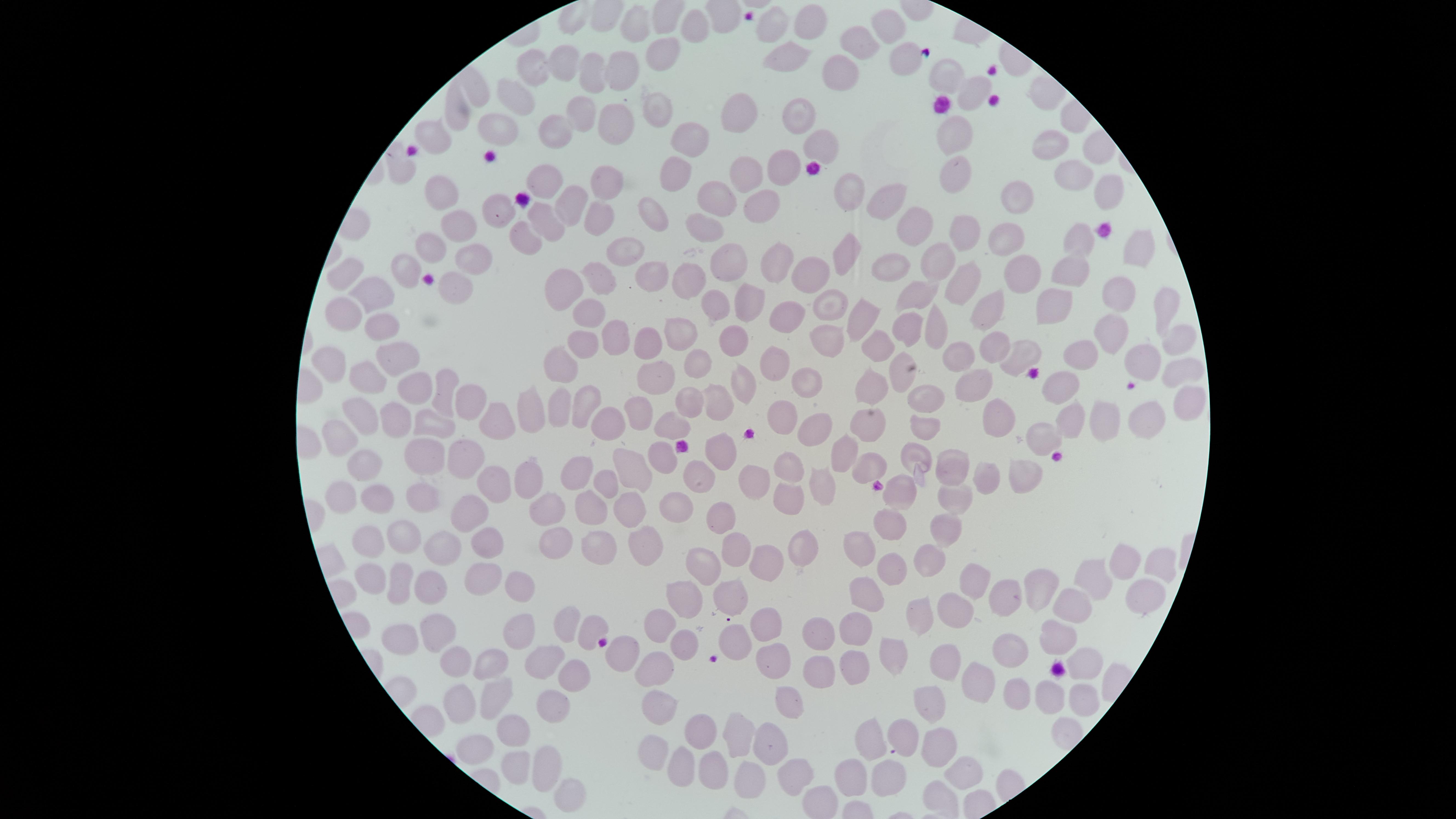

visible region = circular
stain = Giemsa
uninfected RBCs = approximate marker points as (x, y) in pixels: (807, 21), (890, 21), (777, 22), (693, 23), (634, 24), (857, 40), (661, 50), (794, 58), (905, 59), (563, 63), (538, 68), (620, 68), (591, 73), (842, 73), (946, 74), (516, 91), (971, 96), (650, 103), (581, 108), (739, 108), (455, 114), (797, 115), (553, 124), (608, 124), (495, 129), (690, 133), (947, 134), (440, 137), (823, 143), (1051, 145), (401, 166), (784, 169), (746, 174), (955, 175), (677, 177), (1069, 177), (540, 178), (610, 184), (440, 186), (1023, 193), (1113, 194), (719, 196), (840, 196), (761, 199), (879, 201), (570, 203), (502, 205), (654, 214), (548, 218), (599, 218), (915, 219), (459, 226), (709, 229), (1004, 232), (962, 235), (525, 238), (1079, 243), (624, 248), (432, 249), (1136, 253), (476, 256), (847, 256), (936, 256), (727, 261), (776, 262), (893, 267), (1020, 269), (1069, 271), (405, 272), (652, 273), (807, 273), (348, 275), (693, 278), (459, 282), (603, 282), (566, 287), (958, 288), (1116, 293), (372, 295), (922, 296), (838, 302), (1064, 302), (751, 303), (344, 305), (989, 305), (720, 306), (1167, 309), (595, 310), (867, 314), (792, 318), (379, 321), (936, 325), (680, 333), (907, 333), (616, 336), (1114, 337), (737, 338), (1177, 339), (826, 340), (582, 342), (643, 342), (877, 347), (995, 348), (398, 350), (960, 350), (333, 358), (778, 358), (1019, 358), (1085, 358), (700, 362), (1142, 363), (562, 366), (901, 368), (369, 374), (656, 374), (1179, 375), (805, 379), (976, 380), (743, 382), (1060, 383), (412, 387), (440, 391), (875, 394), (468, 398), (926, 399), (1178, 400), (687, 401), (718, 401), (582, 402), (562, 403), (642, 407), (534, 409), (783, 411), (992, 412), (489, 414), (1140, 415), (364, 417), (394, 417), (1062, 417), (1099, 417), (607, 421), (678, 421), (869, 422), (928, 424), (432, 425), (815, 430), (1042, 430), (341, 436), (427, 448), (718, 450), (842, 451), (664, 456), (916, 460), (471, 461), (866, 463), (629, 466), (377, 467), (953, 467), (578, 468), (793, 469), (985, 474), (697, 476), (526, 477), (1024, 477), (499, 480), (754, 481), (603, 482), (823, 489), (900, 491), (425, 494), (350, 496), (379, 499), (949, 499), (466, 502), (546, 503), (785, 504), (674, 506), (630, 512), (719, 513), (593, 514), (888, 521), (406, 524), (945, 527), (363, 535), (547, 539), (478, 543), (645, 543), (443, 544), (734, 545), (858, 545), (799, 547), (602, 551), (930, 557), (766, 564), (364, 570), (706, 570), (890, 570), (1124, 570), (484, 572), (1162, 573), (398, 580), (1094, 582), (972, 583), (432, 585), (1039, 586), (515, 587), (862, 596), (1136, 598), (681, 599), (730, 599), (999, 601), (1076, 608), (962, 612), (916, 616), (660, 622), (853, 623), (444, 624), (563, 624), (403, 626), (764, 626), (590, 627), (516, 633), (819, 633), (1059, 633), (732, 640), (682, 645), (1014, 647), (891, 650), (622, 652), (546, 657), (460, 661), (773, 662), (847, 662), (487, 663), (941, 666), (1081, 667), (660, 670), (818, 677), (569, 678), (976, 680), (1016, 691), (491, 694), (1050, 695), (1081, 696), (660, 701), (453, 705), (552, 706), (787, 707), (927, 708), (509, 729), (700, 732), (733, 734), (902, 737), (869, 741), (938, 743), (470, 745), (773, 745), (652, 746), (547, 764), (681, 764), (712, 765), (515, 770), (960, 770), (792, 776), (745, 777), (884, 777), (845, 779), (562, 791)
capture = smartphone photograph through the microscope eyepiece
image size = 1456×819 pixels
presence = no malaria parasites identified
preparation = thin smear of blood
field of view = single